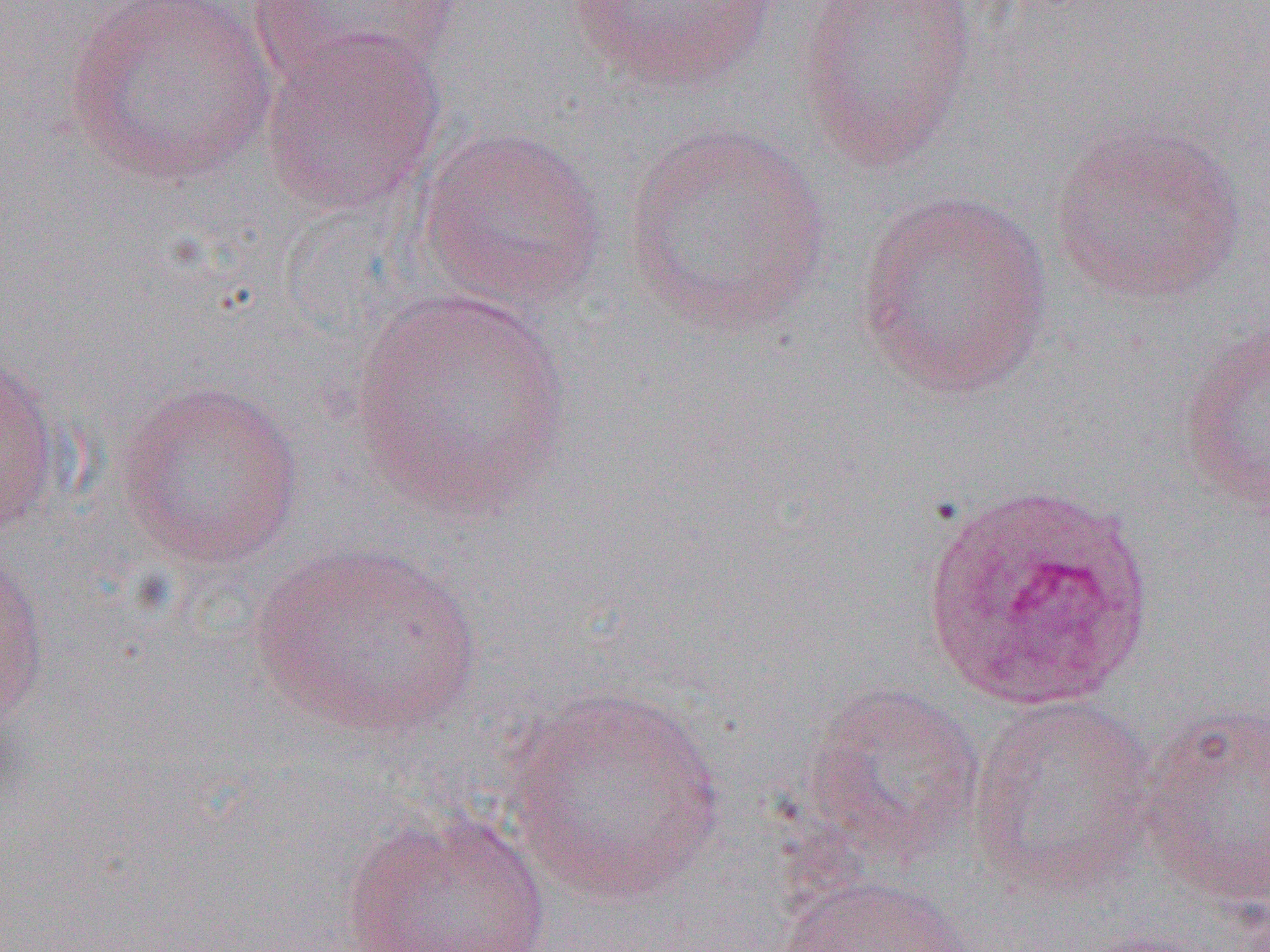
{
  "slide_level_diagnosis": "Plasmodium ovale",
  "modality": "light microscopy",
  "magnification": "1000x",
  "plasmodium_ovale_infected_red_blood_cell_locations": "approximate bounding boxes as (x1,y1)-(x2,y2) corner pairs in pixels: (917,479)-(1157,711)",
  "uninfected_red_blood_cell_locations": "approximate bounding boxes as (x1,y1)-(x2,y2) corner pairs in pixels: (64,0)-(278,187), (251,0)-(467,86), (562,0)-(789,93), (795,0)-(980,172), (256,28)-(447,216), (1048,118)-(1250,306), (622,120)-(832,334), (415,126)-(608,314), (854,189)-(1057,401), (349,287)-(573,519), (1175,315)-(1270,513), (0,353)-(65,537), (114,378)-(306,570), (246,542)-(485,741), (0,550)-(50,728), (799,680)-(986,869), (499,686)-(730,905), (968,693)-(1162,901), (1137,703)-(1269,910), (341,807)-(553,951), (771,875)-(971,951)",
  "image_size": "1270×952 pixels",
  "field_of_view": "single",
  "preparation": "thin blood film"
}